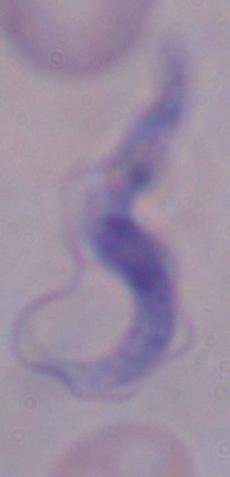
1000x magnification. Photomicrograph. A trypanosome is seen.